State the blood parasite species.
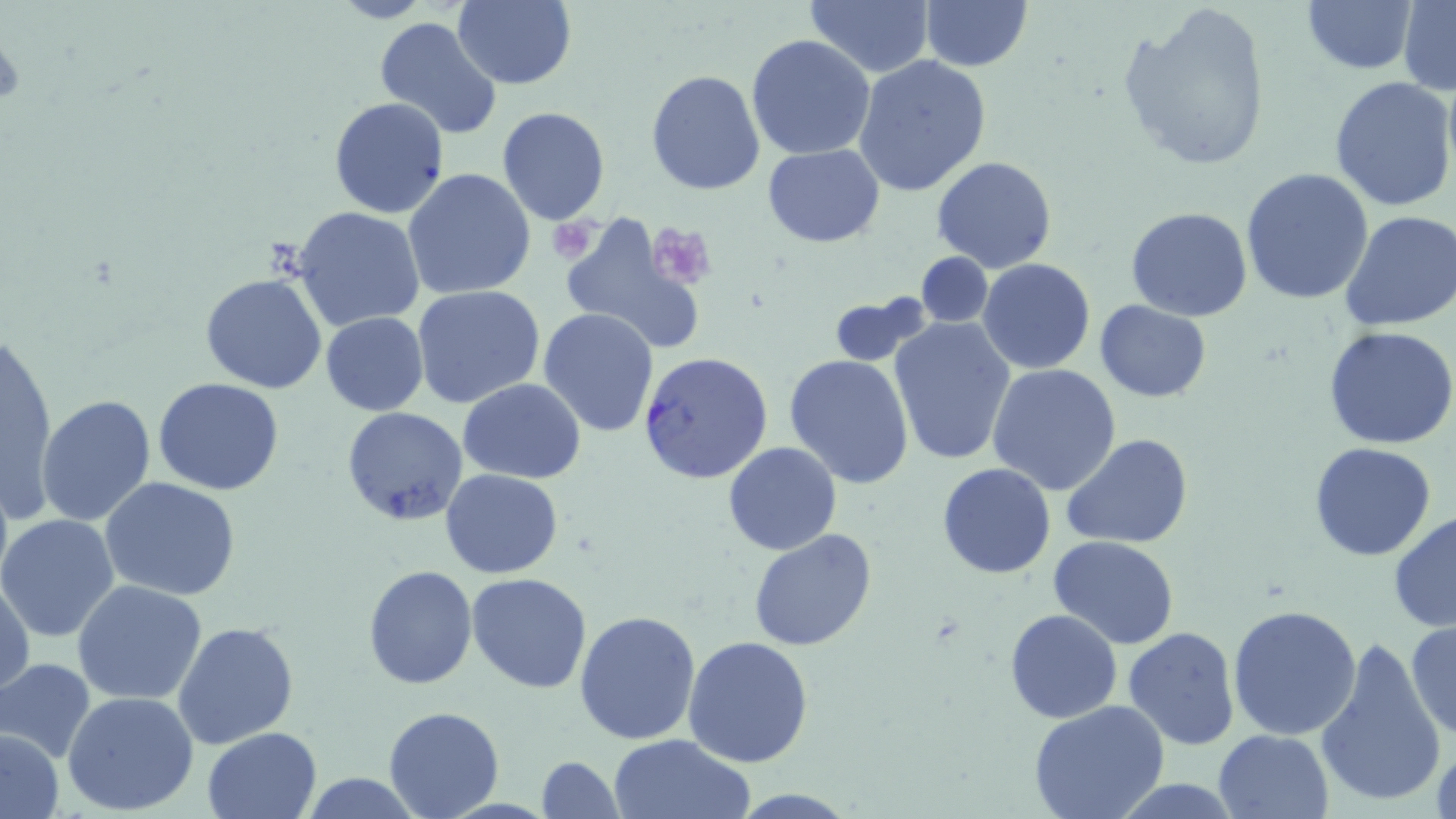
Plasmodium falciparum.

Approximate bounding boxes as (x1,y1)-(x2,y2) corner pairs in pixels. Plasmodium falciparum-infected red blood cell locations: (638,350)-(773,484). Uninfected red blood cell locations: (451,0)-(576,89), (804,0)-(936,78), (1302,1)-(1415,75), (1398,1)-(1456,95), (919,2)-(1032,73), (1119,4)-(1273,171), (374,15)-(502,141), (747,34)-(875,159), (853,54)-(992,196), (646,70)-(766,194), (1329,75)-(1455,213), (329,97)-(450,220), (496,106)-(610,225), (762,144)-(885,246), (932,156)-(1058,273), (402,168)-(536,301), (1240,168)-(1374,305), (1125,206)-(1253,321), (293,207)-(424,331), (1336,209)-(1456,331), (557,217)-(704,353), (915,252)-(994,326), (978,257)-(1095,375), (200,272)-(328,393), (412,286)-(545,411), (828,296)-(927,367), (1095,301)-(1211,403), (538,309)-(659,437), (320,311)-(429,415), (890,317)-(1016,467), (1325,326)-(1456,448), (4,331)-(57,515), (785,354)-(915,488), (987,365)-(1122,495), (153,378)-(285,496), (459,379)-(587,484), (36,395)-(156,527), (341,406)-(469,526), (1061,434)-(1193,550), (723,440)-(842,556), (1309,443)-(1438,562), (936,463)-(1057,580), (441,469)-(563,579), (100,478)-(241,602), (1388,510)-(1456,632), (0,514)-(120,643), (748,528)-(878,651), (1047,536)-(1179,648), (362,565)-(478,689), (467,572)-(594,693), (1,578)-(35,701), (73,580)-(207,704), (1228,602)-(1362,741), (574,609)-(703,745), (1006,610)-(1123,724), (1406,620)-(1455,739), (173,621)-(299,749), (1122,627)-(1240,750), (683,635)-(813,767), (1314,637)-(1447,810), (0,658)-(95,763), (63,690)-(199,815), (1028,700)-(1172,819), (384,705)-(504,817), (202,727)-(323,818), (1,730)-(64,816), (1214,730)-(1332,818), (1428,730)-(1454,819), (607,733)-(755,818), (536,756)-(625,819), (1107,778)-(1246,816), (728,789)-(861,819). Platelet locations: (547,217)-(602,263), (646,223)-(718,289). Image is 1456×819 pixels. Captured at 1000x magnification. Single field of view. May-Grünwald-Giemsa-stained preparation. Thin blood smear. Optical microscopy.